Give the extent of all white blood cells.
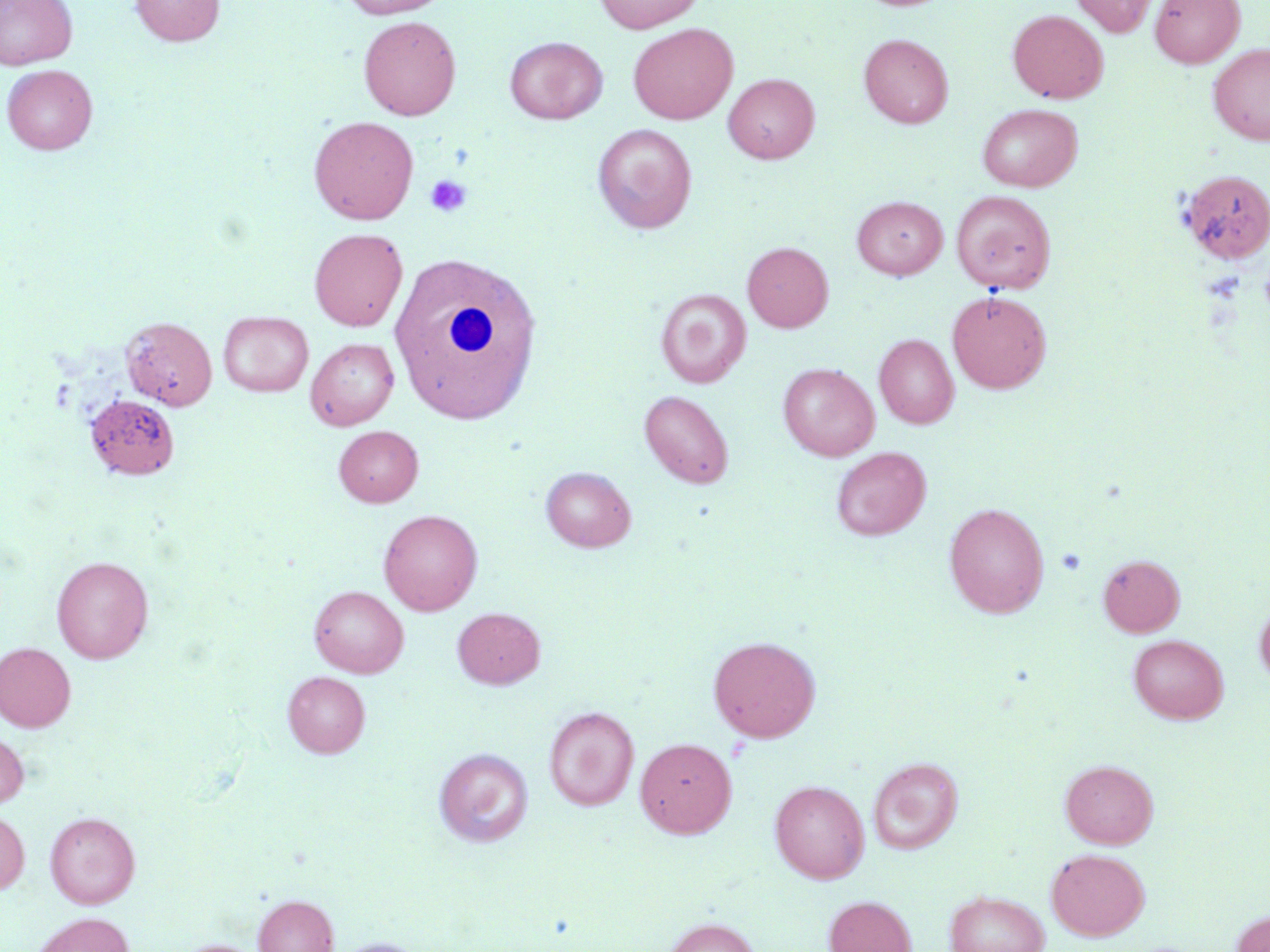

Approximate bounding boxes as (x1,y1)-(x2,y2) corner pairs in pixels.
White blood cells: (388,253)-(543,423).

Summary:
  - Platelet locations: (425,174)-(471,216), (1259,264)-(1270,317), (1056,548)-(1086,575)
  - Uninfected red blood cell locations: (0,0)-(78,70), (130,0)-(225,45), (339,0)-(450,18), (594,0)-(704,33), (1071,0)-(1157,37), (1150,0)-(1245,68), (1008,10)-(1108,103), (358,16)-(461,120), (628,23)-(738,124), (859,33)-(954,128), (504,36)-(607,124), (1207,43)-(1270,146), (2,64)-(98,154), (723,73)-(820,163), (977,103)-(1082,191), (309,115)-(419,224), (593,124)-(698,233), (1179,169)-(1270,263), (952,190)-(1055,293), (852,196)-(947,279), (309,228)-(408,331), (742,242)-(833,333), (655,288)-(751,388), (947,290)-(1051,393), (219,311)-(313,397), (121,316)-(217,410), (874,334)-(959,429), (305,338)-(399,430), (778,362)-(879,461), (639,390)-(734,488), (85,394)-(180,481), (333,425)-(423,507), (831,447)-(931,540), (540,466)-(636,552), (944,502)-(1049,618), (378,509)-(483,616), (1098,554)-(1184,636), (52,555)-(153,663), (309,585)-(409,677), (1254,599)-(1270,688), (453,607)-(545,688), (1127,634)-(1228,724), (708,635)-(821,742), (0,643)-(75,732), (282,671)-(370,757), (543,706)-(639,810), (0,730)-(29,809), (635,737)-(737,838), (433,747)-(533,847), (868,757)-(964,854), (1060,759)-(1158,849), (770,780)-(869,883), (0,810)-(30,894), (44,811)-(140,908), (1046,848)-(1150,940), (944,890)-(1049,952), (253,894)-(338,952), (823,895)-(917,952), (1230,910)-(1270,952), (30,912)-(136,952), (661,917)-(762,952), (328,937)-(432,952), (174,939)-(267,952)
  - Slide-level diagnosis: negative for blood parasites
  - Magnification: 1000x
  - Preparation: thin blood film
  - Image size: 1270×952 pixels
  - Field of view: single
  - Stain: May-Grünwald-Giemsa
  - Modality: light microscopy